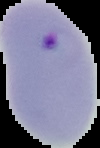

image type = segmented cell region with the area outside set to black
malaria status = parasitized
image size = 100×148 pixels
preparation = thin blood film